Identify the parasite.
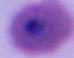
Plasmodium.

modality: photomicrograph
magnification: 400x or 1000x